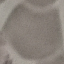
result = negative for malaria parasites
stain = Giemsa
capture = smartphone through the microscope eyepiece
preparation = thin blood film
image type = automatically extracted cell patch, resized to 64 × 64 pixels